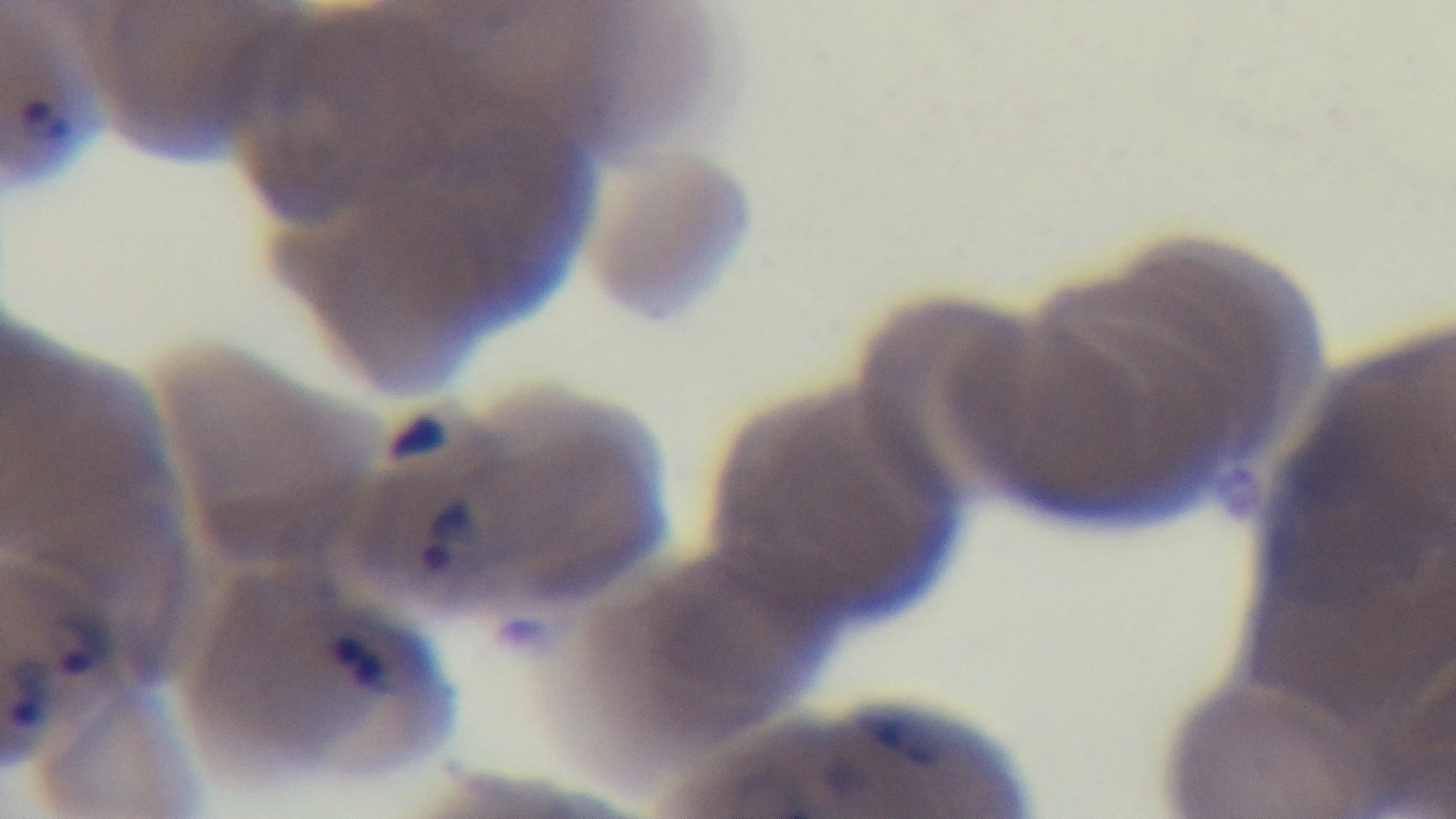
capture: mounted 4K digital camera
objective: 100x oil immersion
malaria_status: infected
preparation: thin
stain: Giemsa
modality: light microscopy
field_of_view: one from the slide